Report the malaria status of this cell.
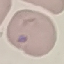
It is parasitized.

Summary:
  - Preparation: thin smear
  - Capture: smartphone through the microscope eyepiece
  - Stain: Giemsa
  - Image type: cell patch, automatically extracted from a larger field of view and resized to 64 × 64 pixels